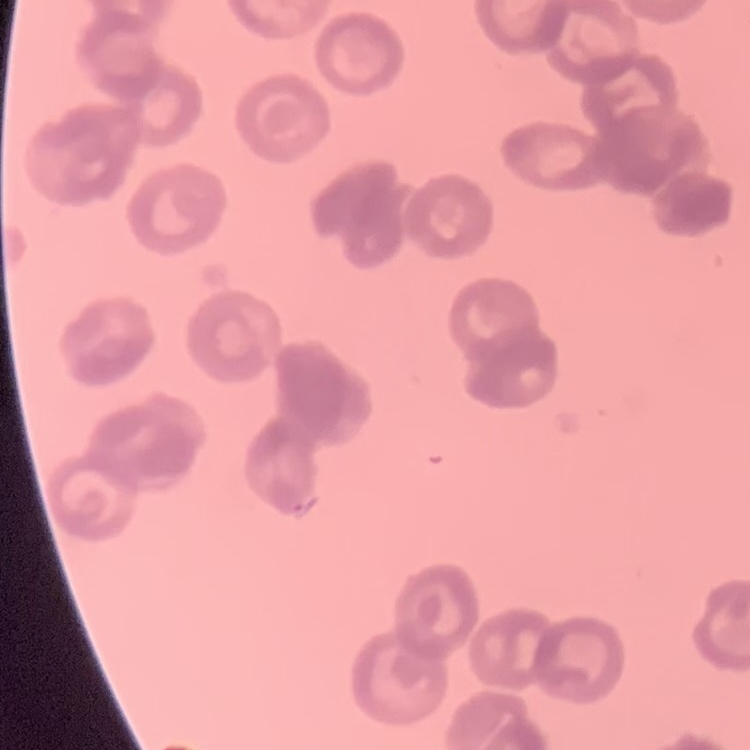
Summary:
  - Erythrocyte morphology: rouleaux formation
  - Image type: square crop of a larger photomicrograph
  - Preparation: thin blood film
  - Stain: Field's or Giemsa